Assess this cell for malaria.
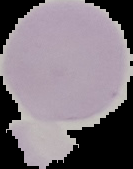
Uninfected.

From a thin blood smear. Image is 133×169 pixels. Segmented cell region on a black background.